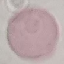
Summary:
  - Malaria status: uninfected
  - Image type: cell patch, automatically extracted from a larger field of view and resized to 64 × 64 pixels
  - Stain: Giemsa
  - Preparation: thin smear
  - Capture: smartphone camera at the microscope eyepiece